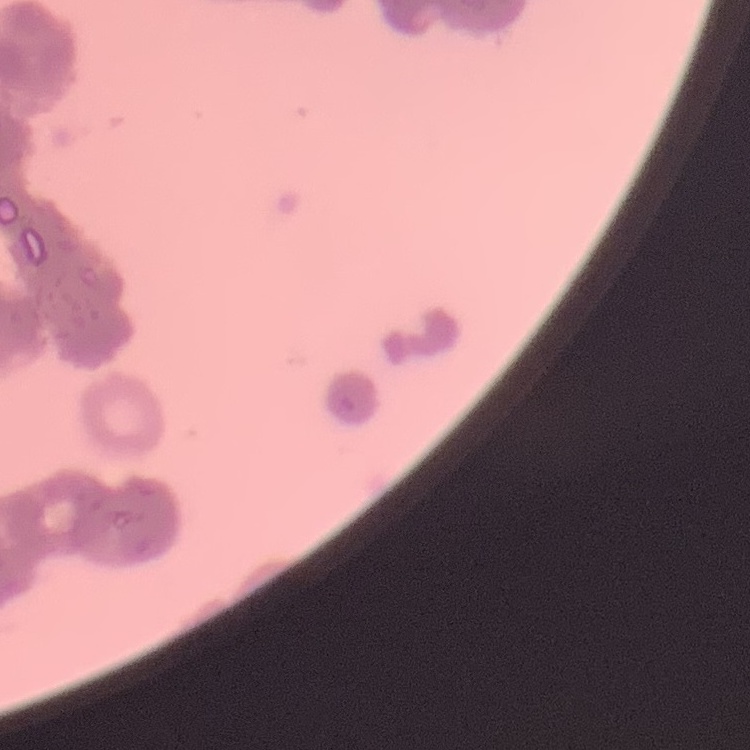 The erythrocytes show rouleaux formation. Field's or Giemsa stain. Square crop of a larger photomicrograph. Thin blood film.